Identify the blood parasite species.
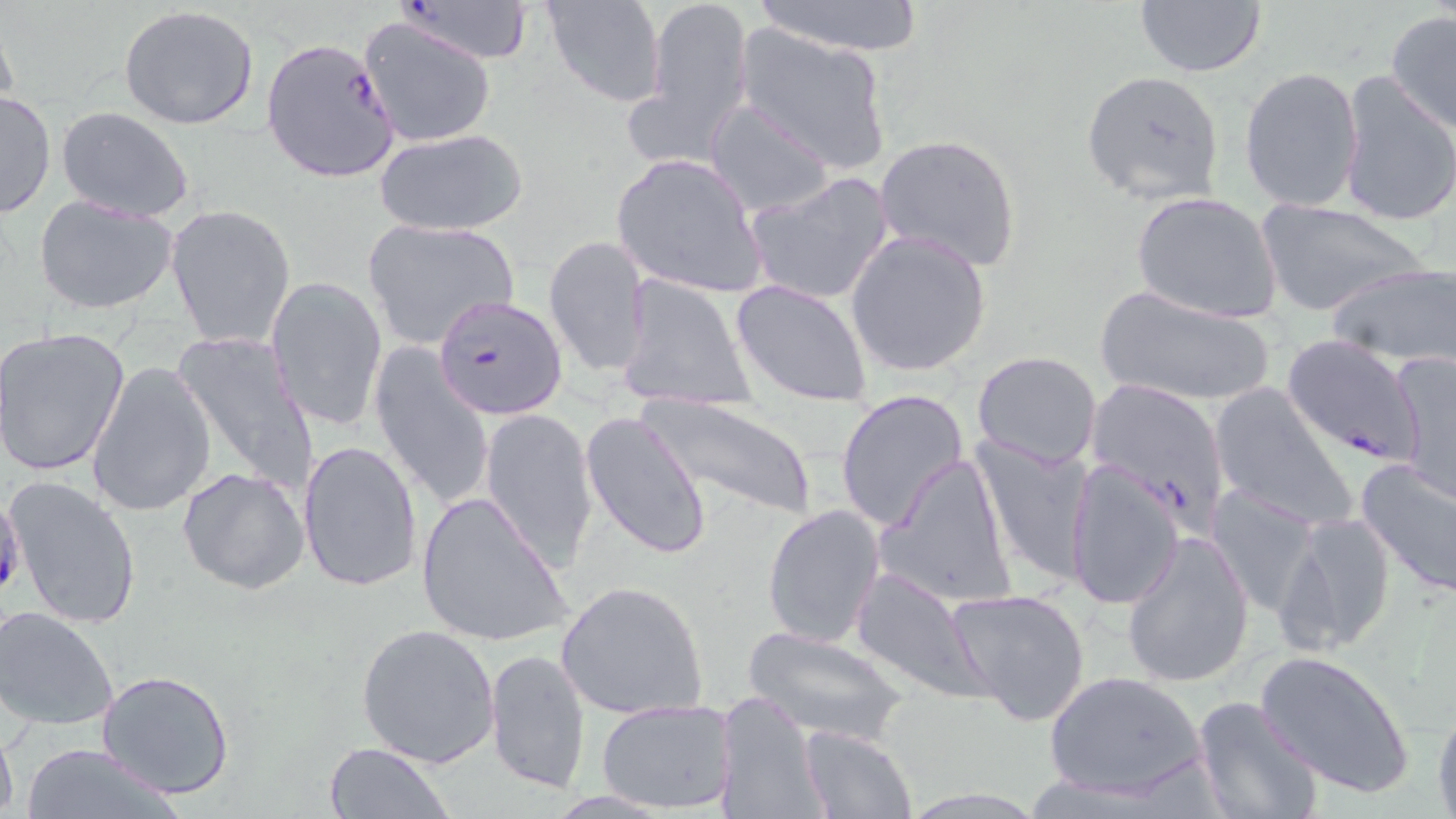

Plasmodium falciparum.

Approximate bounding boxes as (x1,y1)-(x2,y2) corner pairs in pixels. Plasmodium falciparum-infected red blood cell locations: (392,0)-(537,68), (261,36)-(402,183), (433,294)-(568,421), (1281,334)-(1423,468), (1084,377)-(1232,527). Uninfected red blood cell locations: (540,0)-(666,108), (635,0)-(755,165), (748,0)-(927,56), (1133,1)-(1269,78), (117,6)-(262,131), (1385,10)-(1456,135), (358,15)-(497,148), (732,24)-(893,176), (1239,67)-(1365,214), (1080,69)-(1225,205), (1335,69)-(1455,229), (0,90)-(55,220), (704,98)-(837,218), (56,107)-(195,222), (375,129)-(528,238), (874,133)-(1023,272), (609,154)-(766,296), (745,170)-(896,307), (1131,191)-(1285,325), (34,193)-(181,316), (1256,198)-(1429,317), (166,203)-(295,348), (361,218)-(519,349), (845,230)-(992,379), (543,236)-(650,378), (1327,261)-(1456,367), (265,274)-(388,433), (615,274)-(758,410), (732,278)-(875,406), (1094,285)-(1277,410), (1,326)-(132,479), (173,330)-(317,493), (368,346)-(495,512), (971,350)-(1102,468), (1392,351)-(1455,503), (87,360)-(217,517), (1208,383)-(1359,532), (834,388)-(969,532), (639,395)-(818,521), (481,408)-(599,575), (580,412)-(711,560), (971,434)-(1095,585), (298,439)-(420,593), (872,453)-(1018,610), (1354,458)-(1456,600), (1062,460)-(1185,614), (178,466)-(309,595), (2,475)-(141,628), (1205,483)-(1322,619), (1302,488)-(1450,636), (415,490)-(571,647), (762,504)-(886,650), (1276,510)-(1399,658), (1120,530)-(1255,691), (849,568)-(991,704), (556,579)-(709,720), (944,587)-(1094,728), (0,605)-(121,732), (353,622)-(501,768), (742,627)-(907,744), (1256,648)-(1416,799), (484,649)-(593,797), (1043,669)-(1207,801), (97,670)-(235,799), (717,690)-(828,819), (1431,695)-(1456,816), (1192,696)-(1326,819), (594,697)-(737,812), (0,721)-(19,819), (798,726)-(916,818), (322,741)-(456,819), (18,742)-(181,819). Thin blood film. Captured at 1000x magnification. May-Grünwald-Giemsa stain. One field of a larger specimen. Optical microscopy. Image is 1456×819 pixels.